Name the cell type shown.
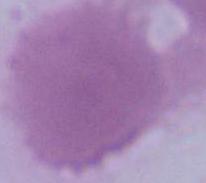
An erythrocyte.

Summary:
  - Modality: photomicrograph
  - Magnification: 1000x